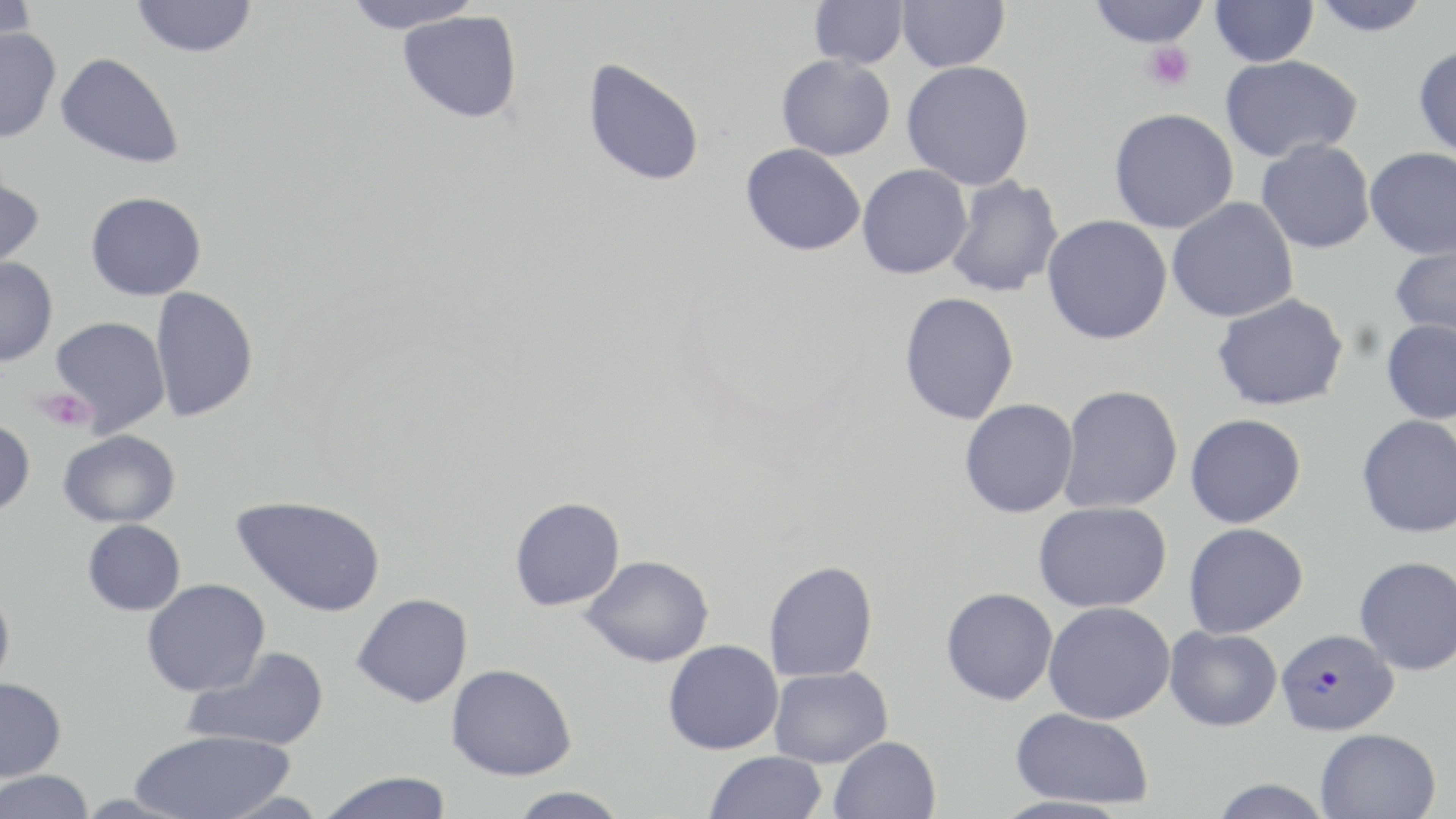

slide-level diagnosis = Plasmodium falciparum
image size = 1456×819 pixels
field of view = single
uninfected red blood cell locations = approximate bounding boxes as [x1, y1, x2, y2] in pixels: [0, 0, 39, 52], [131, 0, 257, 57], [341, 0, 484, 33], [896, 0, 1009, 72], [1089, 0, 1209, 48], [1210, 0, 1319, 66], [1309, 0, 1432, 37], [807, 1, 909, 70], [398, 10, 523, 124], [0, 26, 60, 143], [1412, 43, 1456, 158], [55, 52, 183, 168], [776, 53, 896, 160], [1220, 54, 1363, 163], [582, 58, 706, 187], [901, 60, 1035, 189], [1108, 107, 1239, 234], [1256, 138, 1375, 254], [740, 143, 866, 256], [1364, 146, 1456, 259], [857, 163, 973, 279], [0, 173, 45, 272], [945, 175, 1065, 298], [86, 191, 206, 300], [1166, 197, 1299, 323], [1042, 214, 1172, 345], [1389, 243, 1456, 342], [0, 257, 57, 366], [150, 286, 258, 422], [899, 291, 1019, 425], [1211, 293, 1349, 412], [49, 316, 171, 435], [1381, 318, 1456, 424], [1059, 384, 1184, 513], [959, 398, 1080, 518], [1185, 413, 1306, 528], [1357, 414, 1456, 539], [0, 418, 35, 516], [58, 429, 180, 528], [231, 495, 386, 616], [509, 496, 625, 610], [1033, 501, 1172, 612], [82, 519, 185, 615], [1183, 522, 1308, 638], [581, 555, 713, 667], [1354, 555, 1456, 675], [763, 560, 878, 683], [142, 578, 270, 697], [0, 583, 15, 694], [941, 587, 1058, 705], [351, 593, 473, 707], [1043, 601, 1175, 724], [1165, 625, 1282, 731], [663, 639, 783, 754], [183, 647, 330, 751], [445, 663, 576, 780], [769, 666, 892, 767], [0, 677, 66, 781], [1010, 707, 1155, 810], [130, 728, 295, 819], [1314, 728, 1442, 818], [829, 736, 941, 819], [705, 751, 828, 819], [0, 770, 95, 819], [316, 772, 454, 819], [1207, 779, 1335, 818], [506, 787, 629, 818]
stain = May-Grünwald-Giemsa
magnification = 1000x
Plasmodium falciparum-infected red blood cell locations = approximate bounding boxes as [x1, y1, x2, y2] in pixels: [1276, 628, 1399, 736]
platelet locations = approximate bounding boxes as [x1, y1, x2, y2] in pixels: [1142, 41, 1195, 91], [34, 387, 95, 431]
preparation = thin blood smear
modality = light microscopy